Outline each blood parasite and name the species.
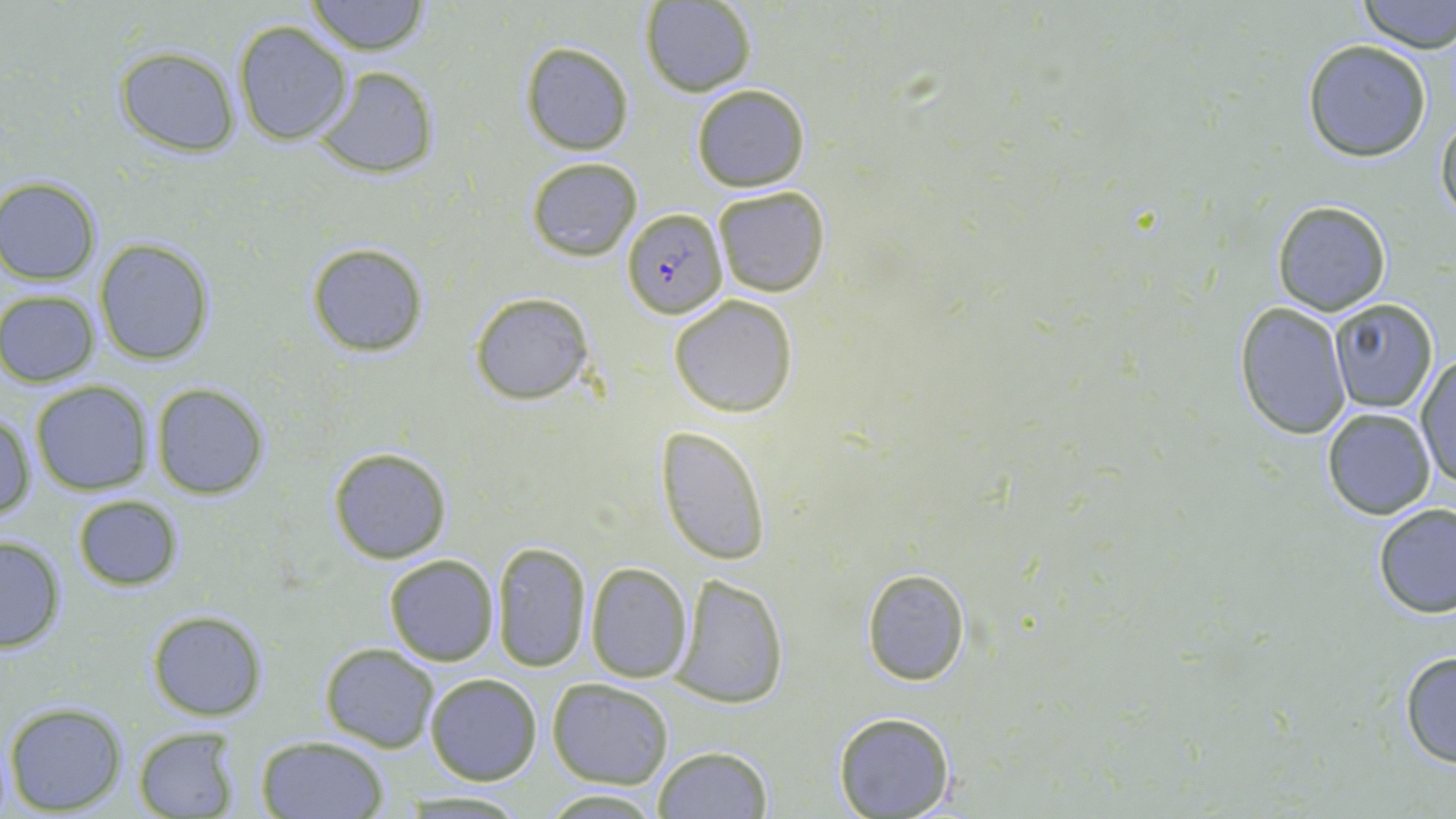

Approximate bounding boxes as named x1/y1/x2/y2 corners in pixels.
Plasmodium falciparum-infected red blood cells: (x1=622, y1=206, x2=724, y2=320).
No Plasmodium ovale, Plasmodium malariae, Plasmodium vivax, Babesia divergens, or Trypanosoma brucei observed.

Uninfected red blood cell locations: (x1=1356, y1=0, x2=1456, y2=52), (x1=306, y1=1, x2=428, y2=55), (x1=640, y1=1, x2=756, y2=96), (x1=233, y1=19, x2=352, y2=145), (x1=1302, y1=39, x2=1433, y2=163), (x1=520, y1=42, x2=634, y2=154), (x1=114, y1=46, x2=241, y2=155), (x1=312, y1=63, x2=440, y2=180), (x1=690, y1=84, x2=811, y2=192), (x1=1436, y1=108, x2=1456, y2=231), (x1=526, y1=156, x2=643, y2=261), (x1=0, y1=176, x2=102, y2=284), (x1=713, y1=184, x2=832, y2=297), (x1=1271, y1=199, x2=1393, y2=316), (x1=95, y1=238, x2=215, y2=366), (x1=306, y1=241, x2=429, y2=358), (x1=1, y1=290, x2=100, y2=386), (x1=470, y1=291, x2=594, y2=406), (x1=668, y1=294, x2=798, y2=419), (x1=1328, y1=300, x2=1438, y2=413), (x1=1234, y1=303, x2=1353, y2=440), (x1=1415, y1=354, x2=1456, y2=492), (x1=30, y1=382, x2=154, y2=495), (x1=150, y1=384, x2=269, y2=499), (x1=1321, y1=406, x2=1435, y2=520), (x1=1, y1=413, x2=36, y2=525), (x1=657, y1=426, x2=771, y2=565), (x1=328, y1=445, x2=454, y2=564), (x1=72, y1=495, x2=184, y2=591), (x1=1372, y1=503, x2=1456, y2=620), (x1=0, y1=534, x2=67, y2=653), (x1=492, y1=540, x2=592, y2=673), (x1=384, y1=553, x2=498, y2=665), (x1=586, y1=563, x2=693, y2=682), (x1=860, y1=567, x2=972, y2=686), (x1=668, y1=572, x2=790, y2=710), (x1=147, y1=610, x2=267, y2=721), (x1=320, y1=644, x2=439, y2=752), (x1=1399, y1=649, x2=1456, y2=767), (x1=423, y1=673, x2=543, y2=786), (x1=547, y1=679, x2=674, y2=787), (x1=3, y1=701, x2=129, y2=815), (x1=833, y1=712, x2=957, y2=819), (x1=131, y1=725, x2=244, y2=819), (x1=253, y1=734, x2=390, y2=818), (x1=652, y1=746, x2=774, y2=819), (x1=540, y1=788, x2=665, y2=817). Slide-level diagnosis: Plasmodium falciparum. Image is 1456×819 pixels. Single field of view. May-Grünwald-Giemsa stain. Thin blood film. Optical microscopy. 1000x magnification.